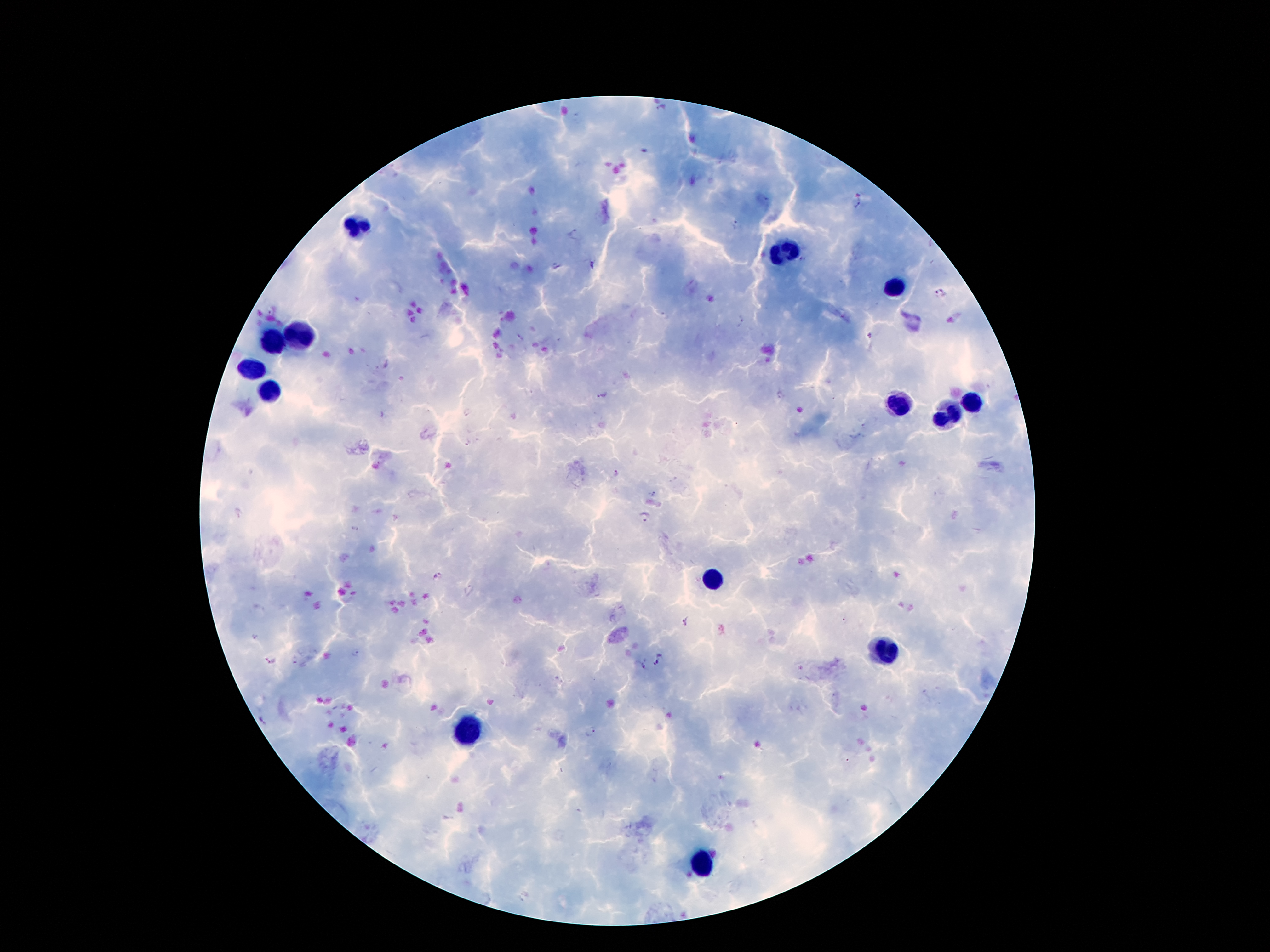

Approximate centers as (x, y) in pixels.
Summary:
  - Leukocyte locations: (355, 224), (786, 252), (892, 285), (305, 332), (271, 346), (251, 369), (266, 389), (971, 399), (898, 406), (948, 417), (712, 577), (882, 651), (465, 729), (701, 862)
  - Malaria parasite locations: (663, 112), (860, 205), (737, 225), (575, 233), (803, 259), (593, 266), (940, 292), (742, 321), (870, 337), (781, 395), (602, 397), (467, 412), (654, 494), (643, 517), (440, 576), (471, 591), (844, 621), (687, 623), (357, 652), (658, 662), (643, 667), (264, 718), (590, 731)
  - Patient malaria status: positive for Plasmodium falciparum
  - Magnification: 100x
  - Field of view: one from this slide
  - Preparation: thick blood film
  - Capture: smartphone through the microscope eyepiece
  - Image size: 1270×952 pixels
  - Stain: Giemsa